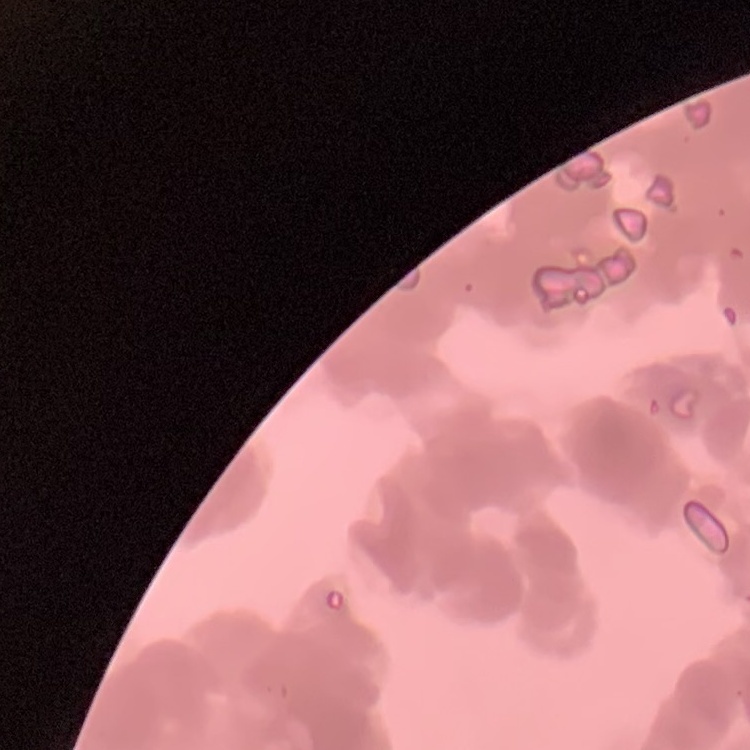
red blood cell morphology = rouleaux formation
image type = one tile cut from a larger photomicrograph
preparation = thin blood smear
stain = Field's or Giemsa